Assess this cell for malaria.
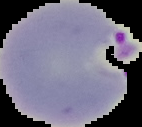

It is parasitized.

preparation = thin blood smear
image type = segmented cell region on a black background
image size = 142×127 pixels